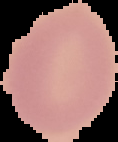

Summary:
  - Preparation: thin blood film
  - Result: negative for Plasmodium parasites
  - Image type: cell region segmented out of the field of view; surrounding area masked to black
  - Image size: 118×142 pixels